State which parasite is depicted.
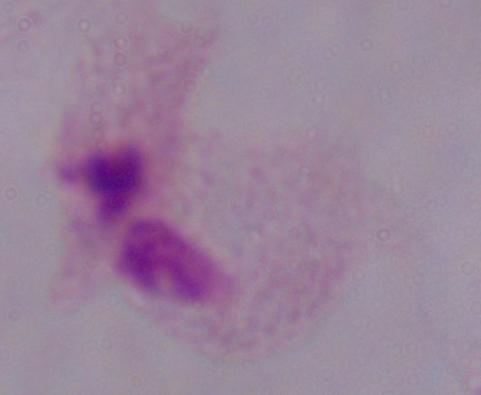

This is a trichomonad.

Captured at 1000x magnification. Photomicrograph.